Point out each leukocyte.
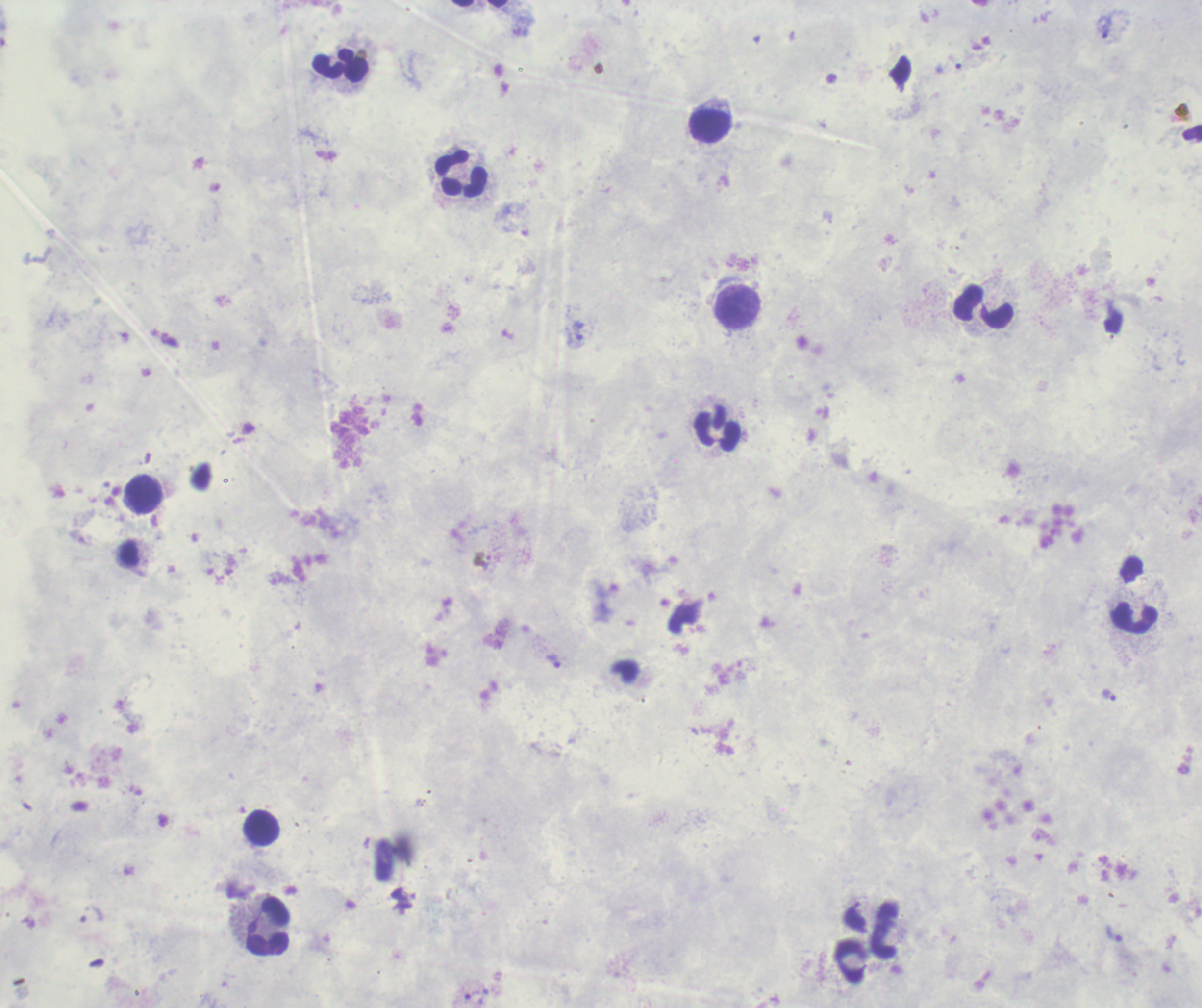

Approximate centers as {x, y} in pixels.
Leukocytes: {341, 65}, {710, 127}, {461, 174}, {738, 307}, {983, 307}, {719, 428}, {143, 494}, {1134, 617}, {260, 828}, {269, 927}, {884, 931}, {850, 961}.

Approximate centers as {x, y} in pixels.
Summary:
  - Trophozoite locations: {1105, 27}, {948, 69}, {579, 331}, {487, 562}, {553, 662}, {1109, 695}, {1113, 934}, {475, 997}
  - Image size: 1202×1008 pixels
  - Result: malaria parasites detected
  - Context: previously used in a real diagnosis
  - Preparation: thick blood film
  - Background quality: poor
  - Stain: Romanowsky
  - Magnification: 100x
  - Field of view: one from this slide